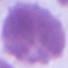 Micrograph. A red blood cell is seen. Captured at 1000x magnification.